Assess this cell for malaria.
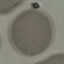

It is uninfected.

Acquired by smartphone through the microscope eyepiece. Automatically extracted cell patch, resized to 64 × 64 pixels. Giemsa-stained preparation. Thin blood film.